Assess this cell for malaria.
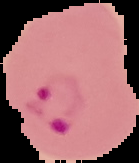

Parasitized.

Summary:
  - Image type: cell region segmented out of the field of view; surrounding area masked to black
  - Image size: 139×163 pixels
  - Preparation: thin blood smear